Describe the morphology of the erythrocytes.
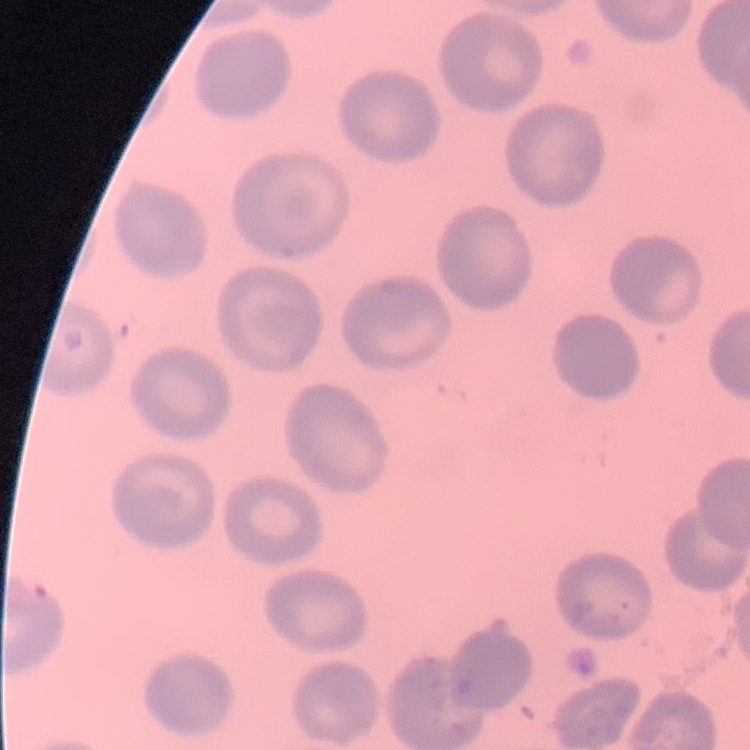

They show no rouleaux formation.

{
  "preparation": "thin blood film",
  "stain": "Field's or Giemsa",
  "image_type": "one tile cut from a larger photomicrograph"
}